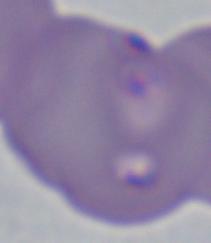

1000x magnification. A Babesia parasite is seen. Photomicrograph.